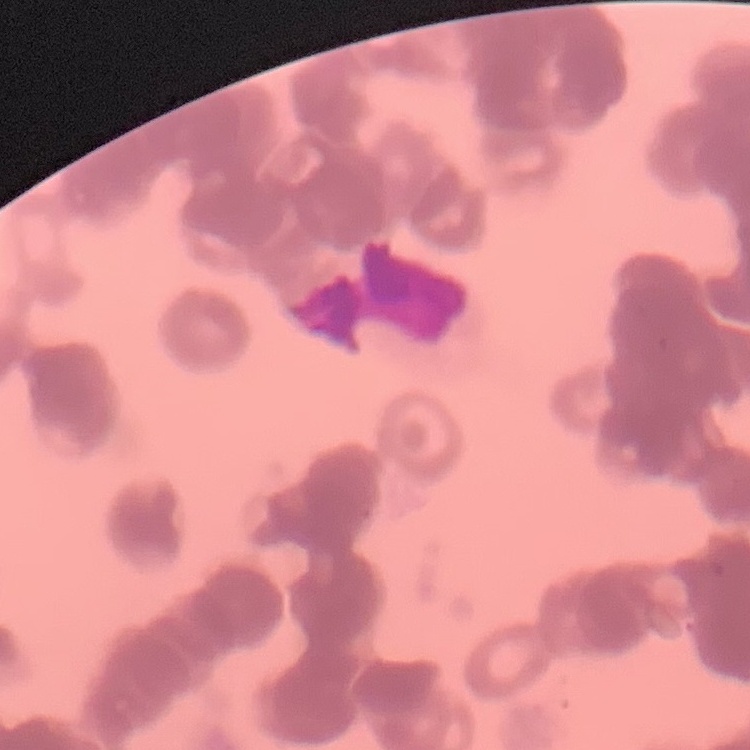
The red blood cells exhibit rouleaux formation. Square crop of a larger photomicrograph. Stained with either Field's or Giemsa. Thin blood smear.